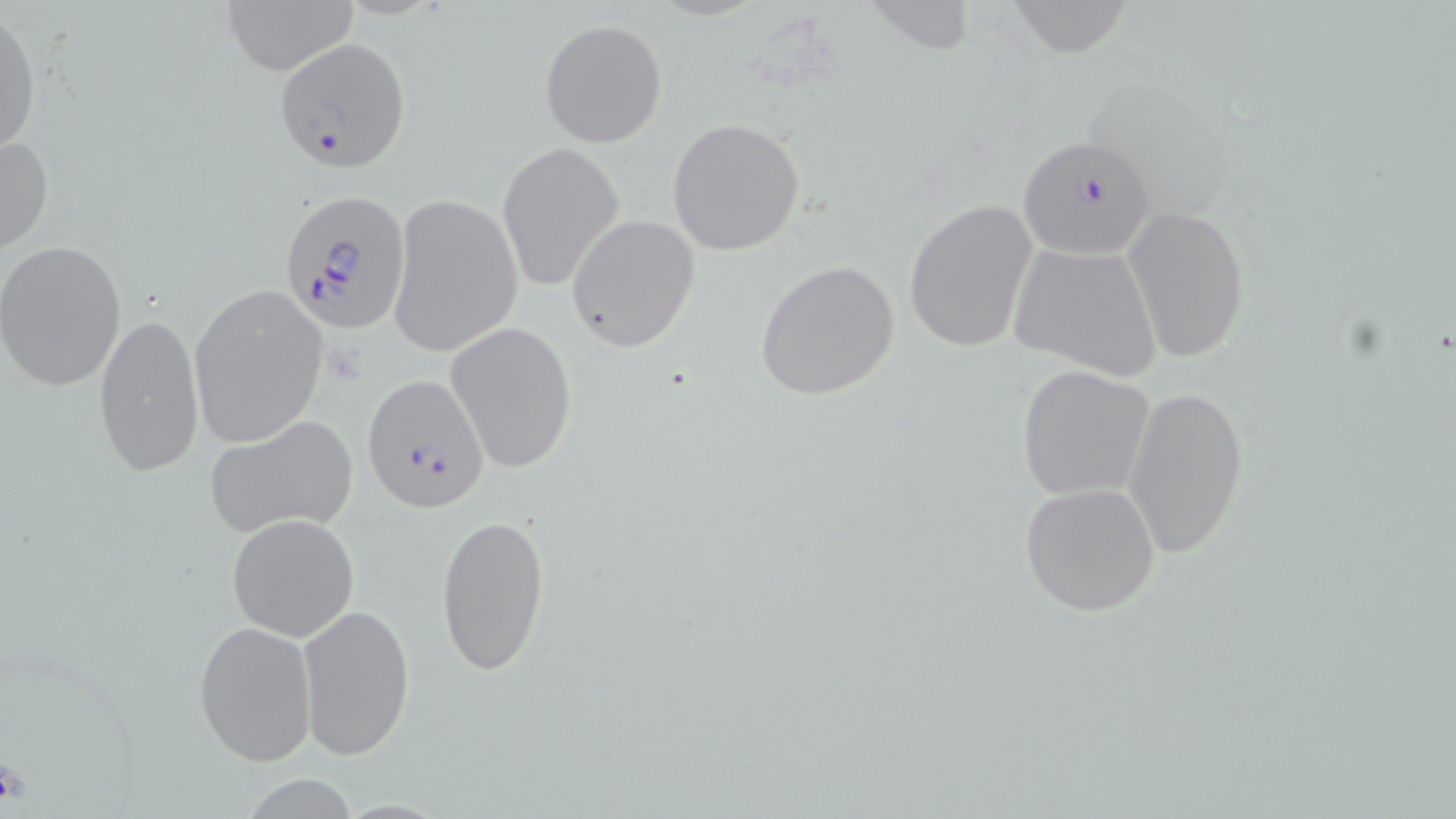
Plasmodium falciparum-infected red blood cell locations = approximate bounding boxes as named x1/y1/x2/y2 corners in pixels: (x1=274, y1=38, x2=412, y2=173), (x1=1017, y1=135, x2=1157, y2=261), (x1=280, y1=190, x2=411, y2=338), (x1=362, y1=374, x2=489, y2=512)
slide-level diagnosis = Plasmodium falciparum
modality = light microscopy
field of view = one of a larger specimen
image size = 1456×819 pixels
stain = May-Grünwald-Giemsa
magnification = 1000x
uninfected red blood cell locations = approximate bounding boxes as named x1/y1/x2/y2 corners in pixels: (x1=216, y1=0, x2=361, y2=75), (x1=1000, y1=0, x2=1134, y2=61), (x1=0, y1=7, x2=41, y2=163), (x1=540, y1=18, x2=667, y2=148), (x1=667, y1=118, x2=806, y2=255), (x1=0, y1=135, x2=52, y2=260), (x1=496, y1=142, x2=623, y2=295), (x1=388, y1=193, x2=521, y2=357), (x1=903, y1=199, x2=1037, y2=354), (x1=1124, y1=204, x2=1249, y2=364), (x1=568, y1=215, x2=700, y2=350), (x1=0, y1=241, x2=127, y2=391), (x1=1008, y1=243, x2=1163, y2=381), (x1=754, y1=258, x2=900, y2=402), (x1=189, y1=286, x2=328, y2=448), (x1=92, y1=311, x2=206, y2=478), (x1=444, y1=320, x2=578, y2=478), (x1=1016, y1=366, x2=1155, y2=500), (x1=1122, y1=381, x2=1249, y2=559), (x1=203, y1=413, x2=359, y2=539), (x1=1020, y1=482, x2=1161, y2=618), (x1=436, y1=510, x2=551, y2=679), (x1=227, y1=513, x2=361, y2=642), (x1=296, y1=602, x2=415, y2=760), (x1=193, y1=619, x2=316, y2=767)
preparation = thin blood film